Describe the morphology of the erythrocytes.
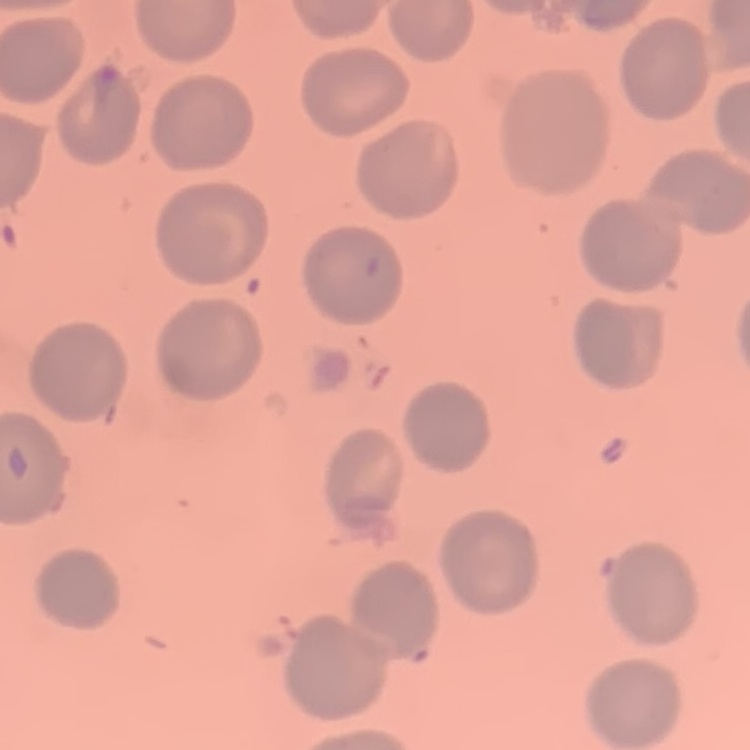

No rouleaux formation.

One tile cut from a larger photomicrograph. Thin blood film. Stained with either Field's or Giemsa.